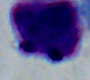
Micrograph. 1000x magnification. A leukocyte is shown.